Assess this cell for malaria.
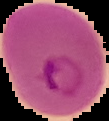
It is parasitized.

Summary:
  - Preparation: thin blood smear
  - Image type: segmented cell region on a black background
  - Image size: 109×121 pixels